Identify the blood parasite species.
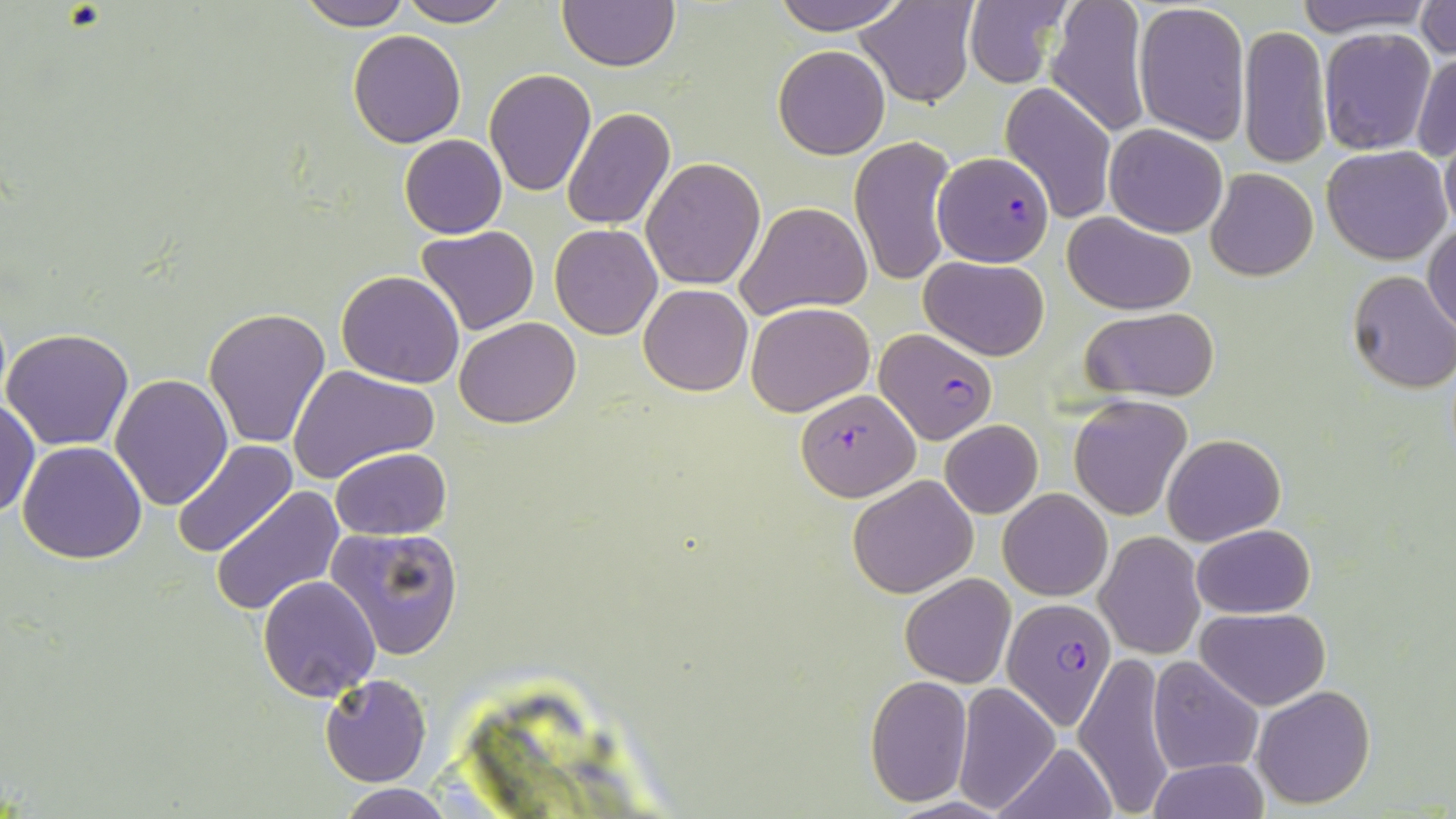
Plasmodium falciparum.

Approximate bounding boxes as (x1, y1, x2, y2) in pixels. Plasmodium falciparum-infected red blood cell locations: (932, 151, 1055, 268), (875, 329, 998, 444), (796, 388, 919, 502), (1004, 598, 1115, 730). Uninfected red blood cell locations: (294, 0, 416, 30), (396, 0, 511, 26), (771, 0, 911, 34), (856, 0, 978, 107), (965, 0, 1073, 88), (1045, 0, 1155, 139), (1290, 0, 1441, 36), (1354, 0, 1456, 53), (557, 1, 679, 71), (1132, 1, 1250, 145), (1415, 1, 1454, 60), (1238, 24, 1332, 170), (1318, 27, 1437, 156), (348, 30, 467, 147), (773, 45, 891, 159), (1412, 51, 1456, 161), (483, 69, 596, 195), (1000, 81, 1117, 226), (561, 107, 676, 231), (1105, 123, 1227, 238), (1440, 127, 1456, 239), (399, 134, 507, 238), (849, 136, 958, 287), (1322, 146, 1453, 266), (640, 158, 766, 289), (1206, 168, 1318, 281), (736, 201, 872, 320), (1063, 213, 1196, 314), (1424, 222, 1456, 334), (550, 224, 662, 340), (416, 226, 541, 335), (920, 255, 1050, 361), (1346, 270, 1456, 393), (336, 271, 466, 388), (639, 283, 753, 396), (746, 302, 875, 416), (1078, 306, 1220, 400), (203, 307, 331, 450), (455, 317, 582, 428), (2, 327, 134, 449), (290, 365, 439, 482), (111, 372, 233, 511), (1069, 395, 1192, 521), (0, 400, 39, 517), (940, 419, 1043, 517), (1162, 433, 1285, 546), (173, 439, 299, 559), (18, 442, 147, 564), (331, 446, 451, 540), (848, 475, 979, 597), (212, 485, 346, 616), (998, 487, 1112, 600), (1193, 524, 1316, 618), (325, 525, 466, 658), (1097, 531, 1205, 659), (899, 573, 1017, 689), (258, 575, 382, 700), (1195, 608, 1330, 711), (1073, 649, 1176, 815), (1147, 658, 1263, 774), (320, 674, 431, 786), (864, 675, 972, 807), (954, 684, 1060, 810), (1251, 684, 1376, 809), (995, 741, 1119, 818), (1147, 759, 1270, 817), (336, 782, 461, 818). One field of a larger specimen. 1000x magnification. May-Grünwald-Giemsa stain. Image is 1456×819 pixels. Thin blood smear. Light microscopy.